State the blood parasite species.
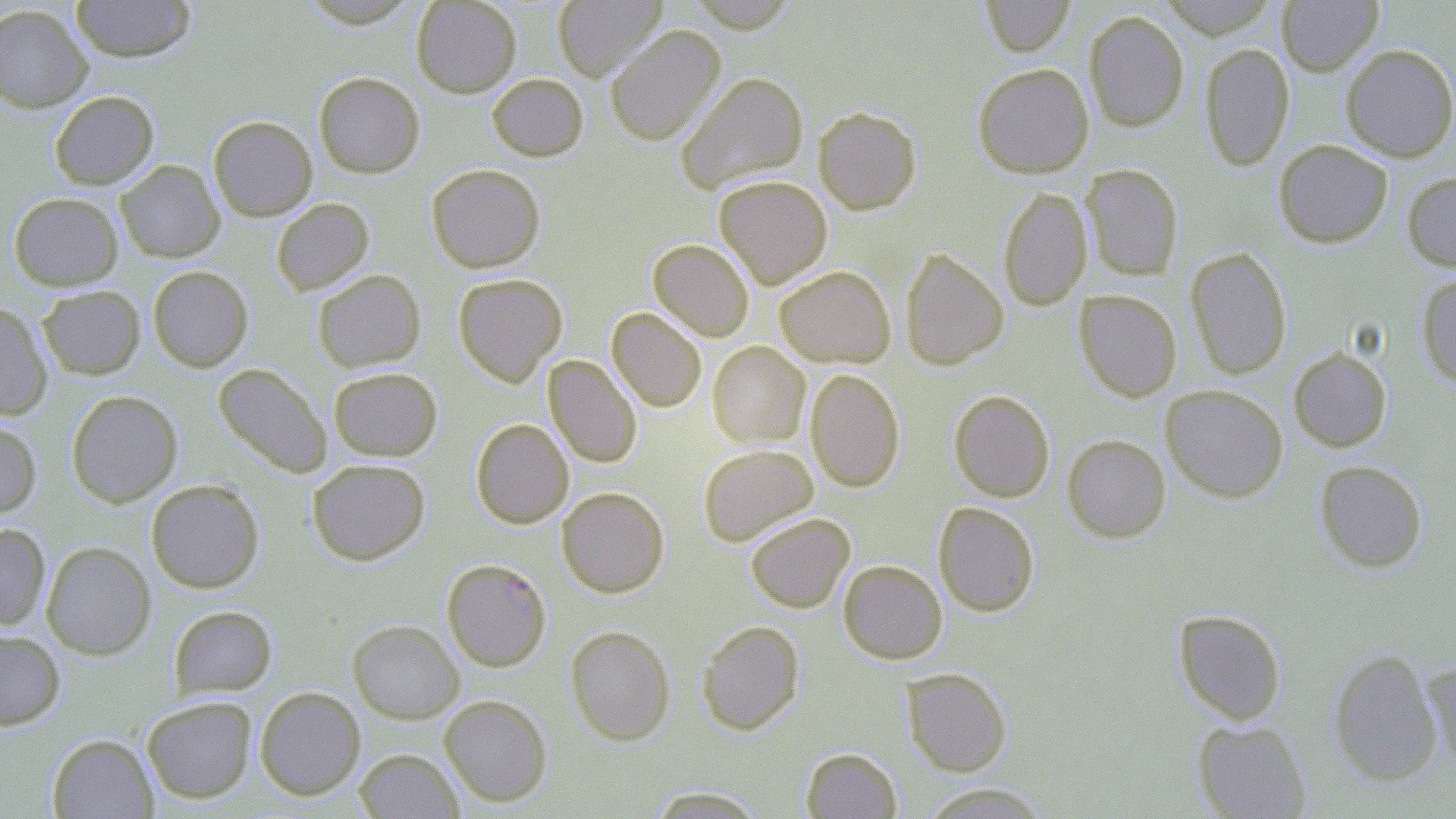

Plasmodium falciparum.

Approximate bounding boxes as (x1, y1, x2, y2) in pixels. Uninfected red blood cell locations: (70, 0, 196, 62), (410, 0, 522, 97), (551, 0, 668, 81), (980, 0, 1076, 56), (1156, 0, 1279, 37), (1276, 0, 1383, 75), (0, 4, 93, 112), (1084, 10, 1189, 131), (604, 24, 725, 145), (1199, 42, 1294, 170), (1340, 44, 1456, 162), (972, 62, 1094, 178), (314, 71, 425, 178), (675, 71, 808, 194), (487, 73, 588, 161), (49, 90, 158, 190), (813, 106, 922, 214), (207, 115, 317, 221), (1273, 139, 1393, 248), (115, 160, 225, 262), (426, 163, 545, 273), (1081, 164, 1183, 280), (1402, 171, 1456, 272), (713, 175, 832, 289), (998, 186, 1092, 310), (8, 192, 123, 290), (271, 197, 374, 295), (648, 239, 754, 341), (1185, 247, 1292, 380), (900, 248, 1008, 370), (147, 265, 253, 372), (774, 266, 896, 367), (312, 269, 426, 373), (453, 273, 568, 386), (1416, 273, 1456, 388), (37, 285, 146, 380), (1074, 289, 1182, 401), (0, 301, 52, 420), (607, 307, 706, 412), (707, 341, 810, 448), (1288, 347, 1392, 451), (543, 355, 642, 468), (212, 363, 333, 478), (328, 366, 442, 461), (805, 368, 905, 492), (1161, 384, 1288, 502), (66, 390, 182, 507), (949, 390, 1055, 502), (470, 418, 574, 528), (0, 421, 41, 520), (1061, 434, 1170, 542), (697, 444, 819, 546), (307, 458, 430, 565), (1314, 460, 1427, 573), (146, 478, 264, 593), (557, 487, 669, 597), (933, 502, 1040, 617), (745, 512, 855, 613), (0, 523, 51, 631), (41, 541, 156, 659), (838, 559, 947, 663), (169, 605, 277, 698), (1173, 609, 1287, 725), (347, 619, 465, 723), (697, 620, 804, 735), (566, 625, 676, 745), (0, 628, 65, 731), (1328, 647, 1442, 786), (1420, 660, 1456, 773), (901, 667, 1012, 777), (254, 686, 366, 800), (439, 694, 552, 807), (142, 696, 257, 803), (1192, 719, 1311, 818), (46, 733, 158, 818), (801, 746, 902, 818), (354, 748, 463, 818), (918, 783, 1052, 818), (646, 786, 767, 817). Plasmodium falciparum-infected red blood cell locations: (441, 557, 552, 671). May-Grünwald-Giemsa stain. 1000x magnification. Thin blood smear. Optical microscopy. One field of a larger specimen. Image is 1456×819 pixels.